Classify this cell by malaria status.
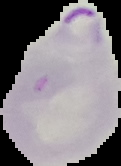
Parasitized.

preparation = thin blood smear
image type = segmented cell region with the area outside set to black
image size = 121×166 pixels